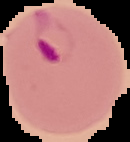
result: Plasmodium parasites identified
image_type: cell region segmented out of the field of view; surrounding area masked to black
preparation: thin blood smear
image_size: 130×142 pixels